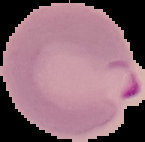

Summary:
  - Preparation: thin blood smear
  - Image type: cell region segmented out of the field of view; surrounding area masked to black
  - Malaria status: parasitized
  - Image size: 145×142 pixels